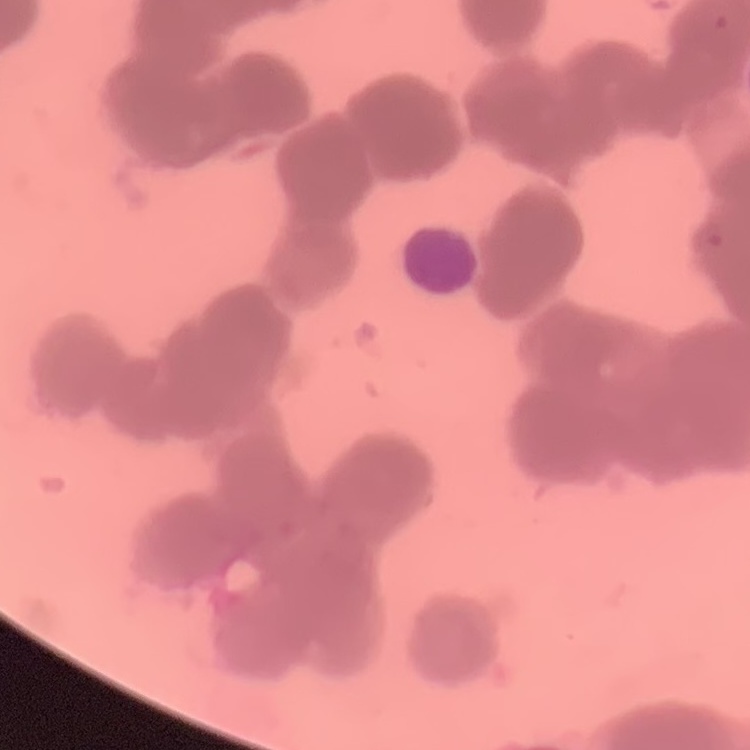

{
  "red_blood_cell_morphology": "rouleaux formation",
  "preparation": "thin blood smear",
  "image_type": "one tile cut from a larger photomicrograph",
  "stain": "Field's or Giemsa"
}